Assess this cell for malaria.
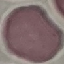

Uninfected.

{
  "capture": "smartphone through the microscope eyepiece",
  "stain": "Giemsa",
  "preparation": "thin blood film",
  "image_type": "automatically extracted cell patch, resized to 64 × 64 pixels"
}